Identify the cell.
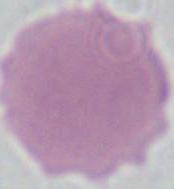
An erythrocyte.

Summary:
  - Magnification: 1000x
  - Modality: photomicrograph